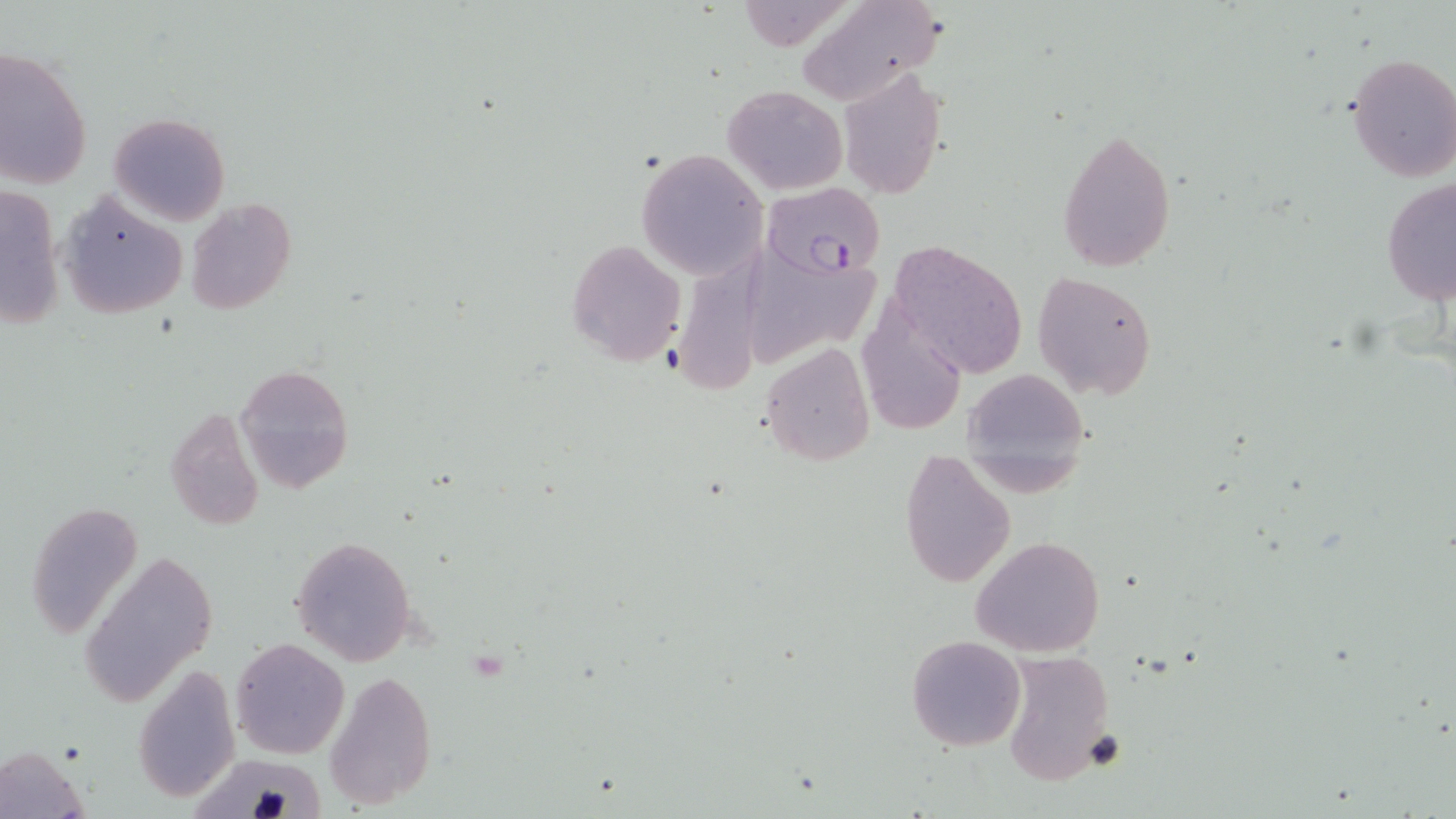
slide-level diagnosis = Plasmodium falciparum
image size = 1456×819 pixels
modality = optical microscopy
field of view = single
Plasmodium falciparum-infected red blood cell locations = approximate bounding boxes as [x1, y1, x2, y2] in pixels: [762, 182, 888, 279]
stain = May-Grünwald-Giemsa
uninfected red blood cell locations = approximate bounding boxes as [x1, y1, x2, y2] in pixels: [795, 0, 946, 103], [1, 49, 92, 188], [1346, 53, 1456, 182], [835, 67, 949, 200], [721, 83, 847, 194], [107, 111, 230, 226], [1056, 128, 1176, 271], [634, 148, 768, 279], [1381, 176, 1456, 305], [2, 182, 64, 327], [57, 190, 186, 318], [187, 199, 296, 316], [566, 238, 688, 368], [887, 239, 1029, 381], [751, 256, 893, 363], [681, 268, 783, 386], [1033, 272, 1156, 400], [855, 300, 970, 438], [759, 341, 875, 467], [234, 363, 356, 494], [961, 365, 1093, 495], [164, 407, 267, 532], [899, 449, 1016, 589], [27, 500, 142, 642], [971, 535, 1106, 658], [289, 536, 416, 665], [82, 550, 218, 705], [906, 634, 1027, 752], [230, 637, 349, 759], [997, 650, 1118, 786], [147, 651, 312, 783], [135, 662, 239, 803], [325, 669, 437, 810], [0, 747, 88, 816]
magnification = 1000x
preparation = thin blood smear